Classify this cell by malaria status.
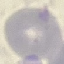

Uninfected.

Automatically extracted cell patch, resized to 64 × 64 pixels. Thin blood smear. Giemsa-stained preparation. Acquired by smartphone through the microscope eyepiece.